Name the blood parasite species.
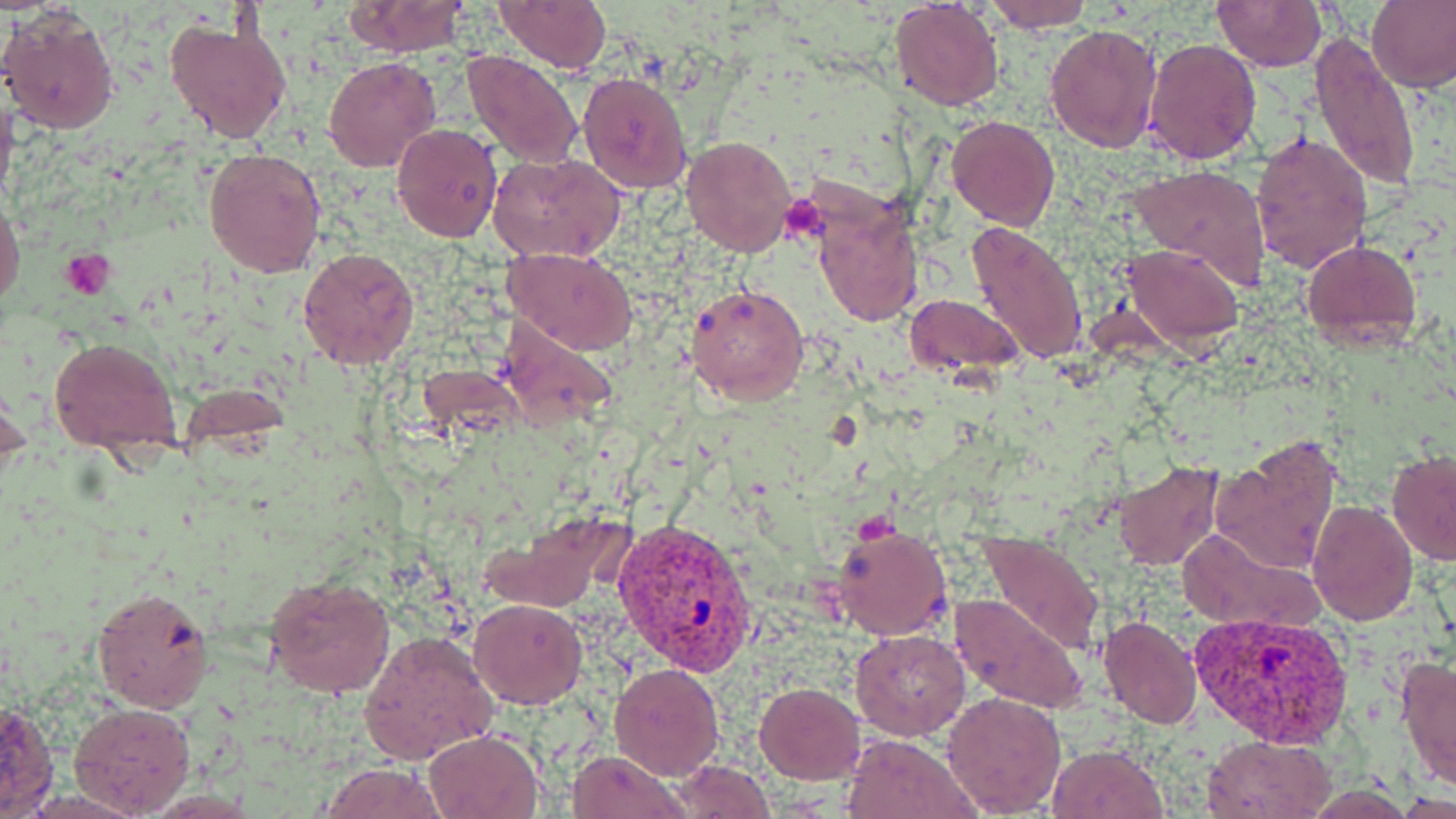
Plasmodium vivax.

{
  "platelet_locations": "approximate bounding boxes as named x1/y1/x2/y2 corners in pixels: (x1=779, y1=194, x2=829, y2=245), (x1=61, y1=250, x2=112, y2=300)",
  "magnification": "1000x",
  "plasmodium_vivax_infected_red_blood_cell_locations": "approximate bounding boxes as named x1/y1/x2/y2 corners in pixels: (x1=613, y1=516, x2=756, y2=674), (x1=1186, y1=610, x2=1357, y2=746)",
  "stain": "May-Grünwald-Giemsa",
  "image_size": "1456×819 pixels",
  "uninfected_red_blood_cell_locations": "approximate bounding boxes as named x1/y1/x2/y2 corners in pixels: (x1=984, y1=0, x2=1093, y2=33), (x1=1211, y1=0, x2=1327, y2=72), (x1=1368, y1=0, x2=1456, y2=93), (x1=341, y1=1, x2=471, y2=57), (x1=494, y1=1, x2=611, y2=73), (x1=893, y1=2, x2=1004, y2=110), (x1=0, y1=7, x2=121, y2=136), (x1=164, y1=17, x2=294, y2=144), (x1=1043, y1=24, x2=1162, y2=154), (x1=1309, y1=33, x2=1419, y2=194), (x1=1143, y1=38, x2=1262, y2=165), (x1=462, y1=49, x2=582, y2=168), (x1=323, y1=57, x2=441, y2=173), (x1=577, y1=69, x2=693, y2=195), (x1=0, y1=87, x2=18, y2=214), (x1=947, y1=115, x2=1060, y2=230), (x1=392, y1=123, x2=502, y2=242), (x1=1249, y1=132, x2=1372, y2=273), (x1=681, y1=135, x2=798, y2=258), (x1=204, y1=147, x2=327, y2=279), (x1=488, y1=151, x2=625, y2=260), (x1=1127, y1=164, x2=1273, y2=290), (x1=812, y1=199, x2=924, y2=329), (x1=0, y1=200, x2=24, y2=310), (x1=966, y1=222, x2=1088, y2=366), (x1=1302, y1=239, x2=1420, y2=350), (x1=1122, y1=244, x2=1244, y2=349), (x1=298, y1=246, x2=420, y2=370), (x1=505, y1=246, x2=638, y2=354), (x1=690, y1=282, x2=810, y2=407), (x1=904, y1=293, x2=1024, y2=377), (x1=47, y1=336, x2=182, y2=456), (x1=0, y1=379, x2=29, y2=484), (x1=1210, y1=435, x2=1342, y2=578), (x1=1386, y1=450, x2=1456, y2=564), (x1=1114, y1=460, x2=1225, y2=572), (x1=1225, y1=463, x2=1395, y2=609), (x1=1306, y1=500, x2=1417, y2=625), (x1=478, y1=510, x2=631, y2=613), (x1=832, y1=523, x2=953, y2=641), (x1=1175, y1=525, x2=1320, y2=632), (x1=977, y1=533, x2=1105, y2=655), (x1=264, y1=572, x2=397, y2=698), (x1=91, y1=586, x2=215, y2=712), (x1=950, y1=592, x2=1086, y2=713), (x1=469, y1=599, x2=587, y2=709), (x1=1098, y1=614, x2=1202, y2=729), (x1=850, y1=629, x2=970, y2=740), (x1=357, y1=630, x2=498, y2=765), (x1=1396, y1=655, x2=1456, y2=791), (x1=609, y1=663, x2=724, y2=780), (x1=755, y1=683, x2=866, y2=783), (x1=940, y1=690, x2=1067, y2=816), (x1=0, y1=700, x2=59, y2=818), (x1=68, y1=702, x2=195, y2=815), (x1=424, y1=728, x2=544, y2=819), (x1=842, y1=732, x2=980, y2=819), (x1=1202, y1=735, x2=1335, y2=818), (x1=1047, y1=744, x2=1168, y2=819), (x1=567, y1=748, x2=686, y2=819), (x1=670, y1=760, x2=774, y2=817), (x1=317, y1=762, x2=450, y2=819)",
  "field_of_view": "one of a larger specimen",
  "preparation": "thin blood smear",
  "modality": "light microscopy"
}